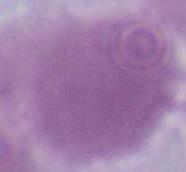 A red blood cell is seen. 1000x magnification. Photomicrograph.